State which parasite is depicted.
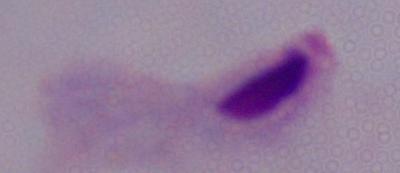

A trichomonad.

modality = micrograph
magnification = 1000x